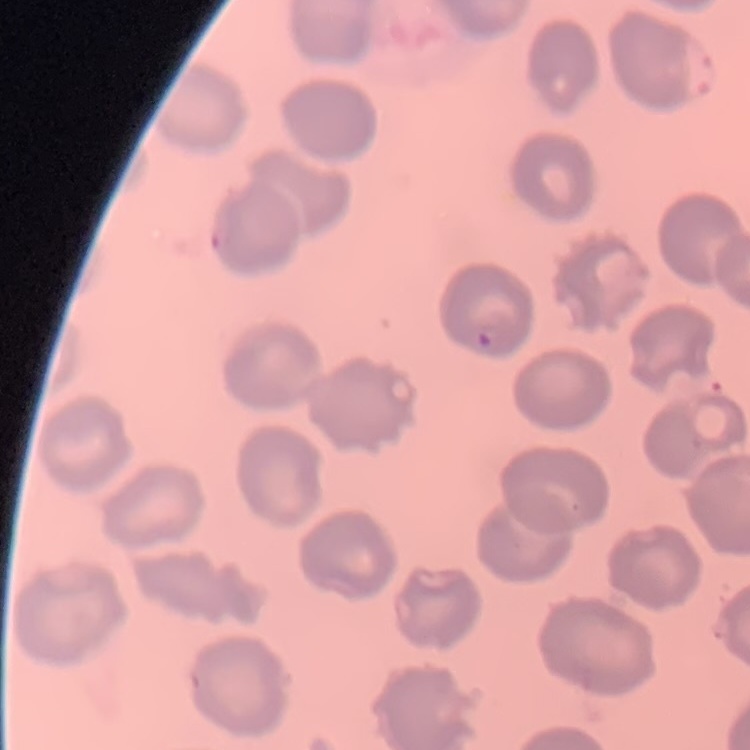

Summary:
  - Erythrocyte morphology: no rouleaux formation
  - Image type: square crop of a larger photomicrograph
  - Stain: Field's or Giemsa
  - Preparation: thin blood smear